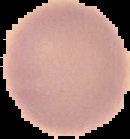
image_size: 130×139 pixels
image_type: cell region segmented out of the field of view; surrounding area masked to black
malaria_status: uninfected
preparation: thin blood film